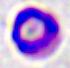

Summary:
  - Modality: photomicrograph
  - Magnification: 400x
  - Identification: white blood cell